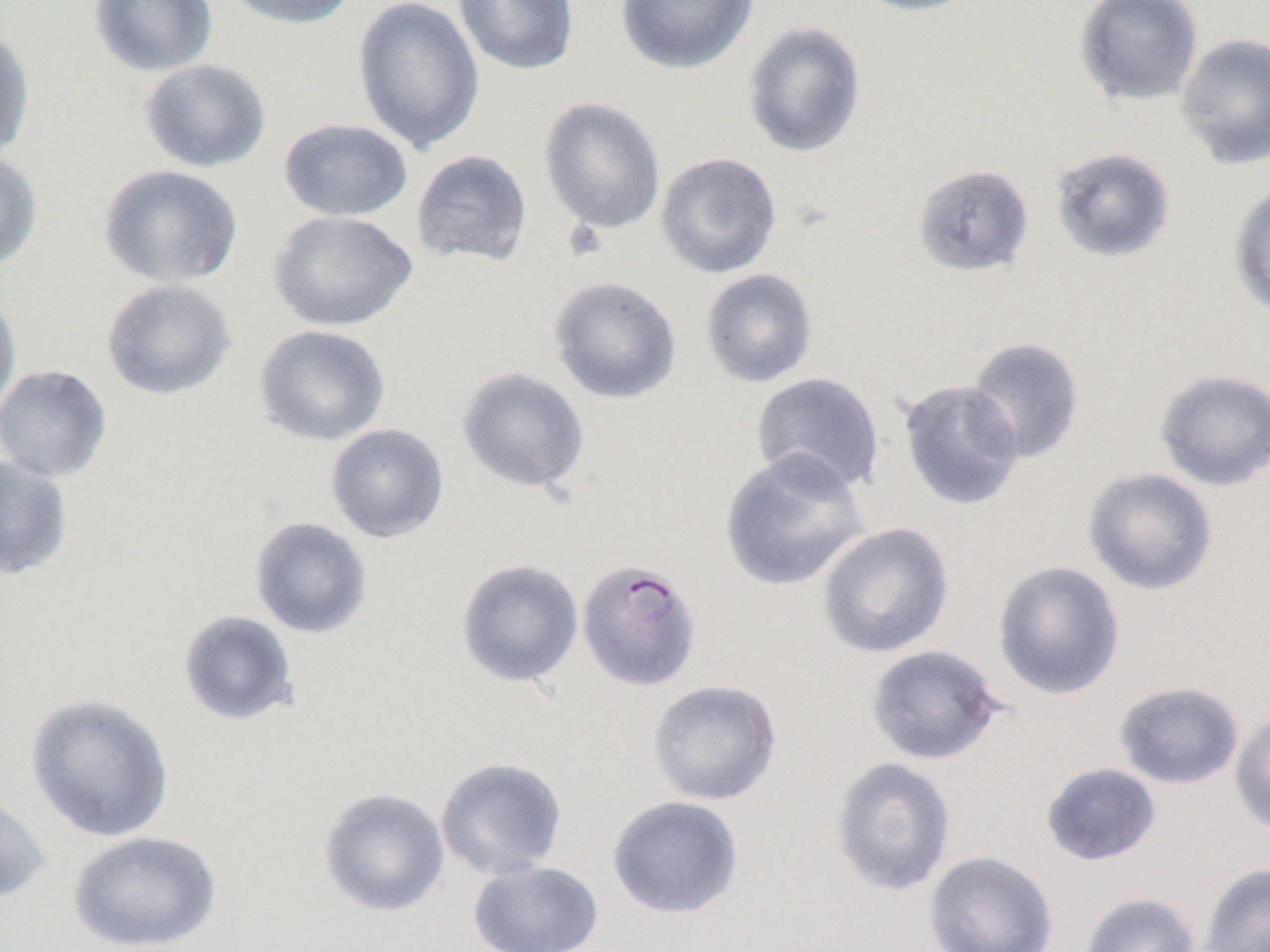

Approximate bounding boxes as named x1/y1/x2/y2 corners in pixels. Uninfected red blood cell locations: (x1=89, y1=0, x2=218, y2=76), (x1=217, y1=0, x2=360, y2=30), (x1=352, y1=0, x2=485, y2=155), (x1=452, y1=0, x2=580, y2=76), (x1=615, y1=0, x2=759, y2=75), (x1=849, y1=0, x2=982, y2=17), (x1=1073, y1=0, x2=1204, y2=107), (x1=742, y1=21, x2=867, y2=159), (x1=0, y1=25, x2=35, y2=162), (x1=1176, y1=32, x2=1270, y2=170), (x1=139, y1=58, x2=272, y2=173), (x1=538, y1=96, x2=667, y2=235), (x1=278, y1=118, x2=414, y2=222), (x1=1050, y1=146, x2=1176, y2=262), (x1=410, y1=149, x2=533, y2=267), (x1=0, y1=150, x2=43, y2=272), (x1=655, y1=151, x2=782, y2=279), (x1=913, y1=164, x2=1035, y2=277), (x1=98, y1=165, x2=243, y2=289), (x1=1228, y1=183, x2=1270, y2=320), (x1=268, y1=210, x2=418, y2=332), (x1=699, y1=268, x2=819, y2=389), (x1=547, y1=275, x2=682, y2=405), (x1=101, y1=278, x2=237, y2=401), (x1=0, y1=289, x2=22, y2=420), (x1=252, y1=324, x2=392, y2=448), (x1=965, y1=336, x2=1085, y2=464), (x1=0, y1=364, x2=113, y2=483), (x1=455, y1=366, x2=590, y2=494), (x1=1154, y1=367, x2=1270, y2=491), (x1=750, y1=372, x2=885, y2=494), (x1=897, y1=379, x2=1026, y2=511), (x1=325, y1=423, x2=449, y2=544), (x1=718, y1=448, x2=870, y2=592), (x1=0, y1=455, x2=74, y2=581), (x1=1082, y1=467, x2=1219, y2=596), (x1=249, y1=516, x2=373, y2=640), (x1=816, y1=521, x2=955, y2=660), (x1=455, y1=558, x2=584, y2=688), (x1=991, y1=559, x2=1126, y2=701), (x1=177, y1=610, x2=300, y2=727), (x1=865, y1=644, x2=1005, y2=766), (x1=647, y1=679, x2=782, y2=806), (x1=1114, y1=680, x2=1245, y2=790), (x1=24, y1=692, x2=175, y2=843), (x1=1230, y1=710, x2=1270, y2=839), (x1=830, y1=756, x2=957, y2=897), (x1=435, y1=757, x2=568, y2=881), (x1=1040, y1=762, x2=1162, y2=866), (x1=317, y1=787, x2=450, y2=918), (x1=0, y1=792, x2=52, y2=906), (x1=606, y1=796, x2=744, y2=919), (x1=67, y1=830, x2=222, y2=952), (x1=925, y1=850, x2=1058, y2=952), (x1=467, y1=860, x2=605, y2=952), (x1=1199, y1=862, x2=1270, y2=952), (x1=1079, y1=893, x2=1201, y2=952). Plasmodium falciparum-infected red blood cell locations: (x1=576, y1=557, x2=703, y2=691). Slide-level diagnosis: Plasmodium falciparum. Light microscopy. Single field of view. Thin blood smear. 1000x magnification. Image is 1270×952 pixels.